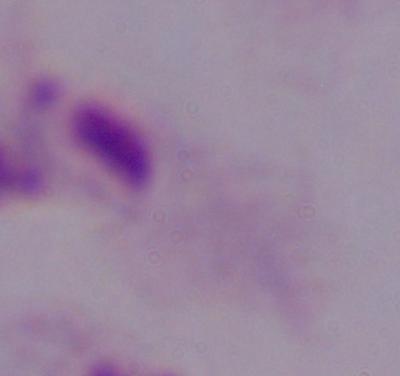

Summary:
  - Identification: trichomonad
  - Magnification: 1000x
  - Modality: photomicrograph